Classify this cell by malaria status.
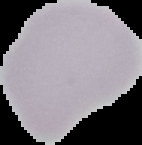

It is uninfected.

Cell region segmented out of the field of view; the surrounding area is masked to black. Image is 142×145 pixels. From a thin blood smear.